Report the malaria status of this cell.
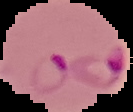

Parasitized.

Cell region segmented out of the field of view; the surrounding area is masked to black. Image is 133×112 pixels. From a thin blood smear.